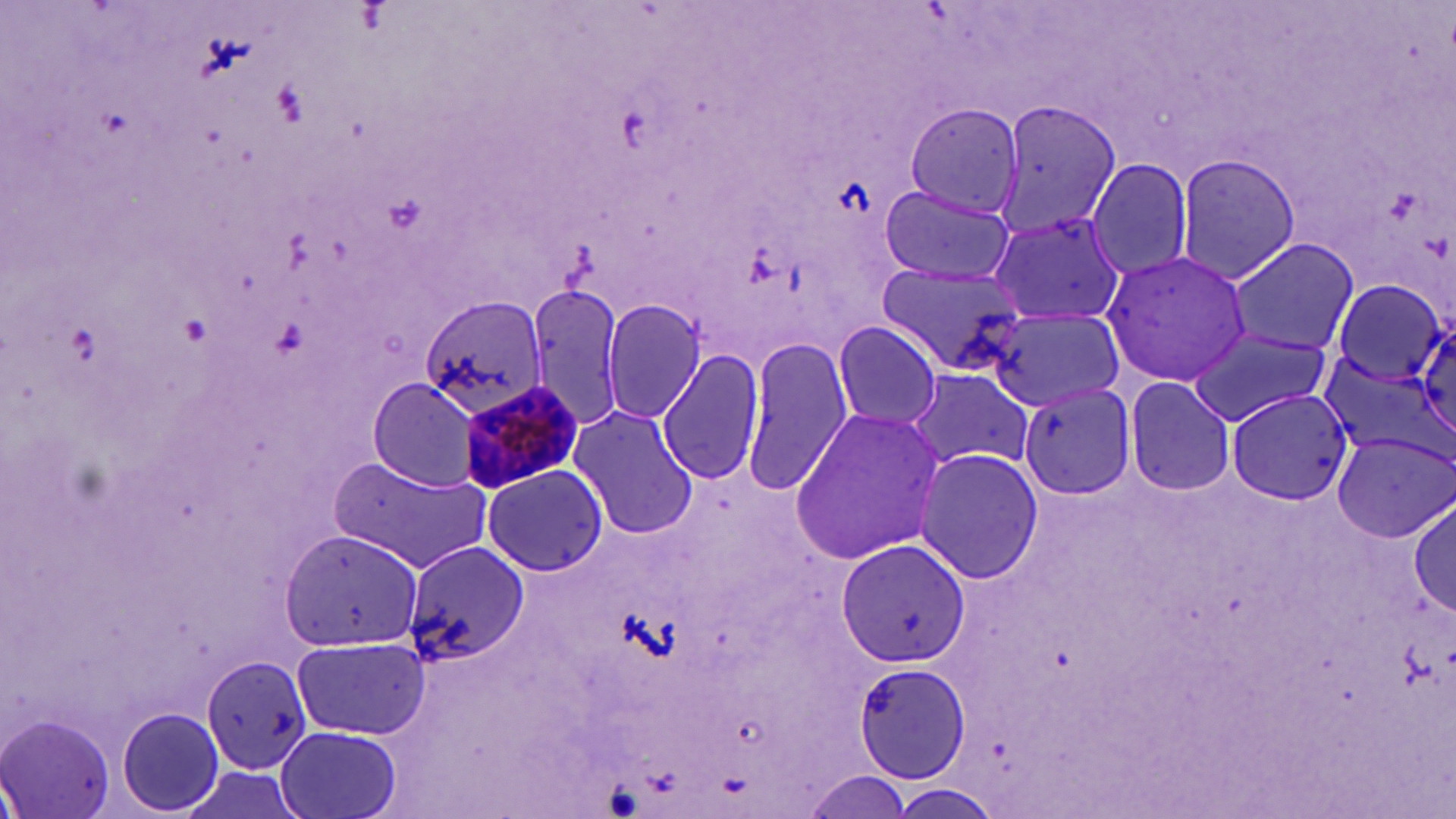 Approximate bounding boxes as [x1, y1, x2, y2] in pixels. Plasmodium malariae-infected red blood cell locations: [456, 379, 587, 496]. Uninfected red blood cell locations: [991, 98, 1120, 241], [903, 102, 1022, 220], [902, 104, 1023, 217], [1174, 153, 1301, 284], [1087, 157, 1195, 281], [879, 185, 1016, 285], [987, 210, 1126, 327], [1224, 237, 1357, 357], [1100, 250, 1252, 388], [875, 260, 1033, 378], [1330, 279, 1447, 385], [525, 282, 625, 432], [420, 294, 551, 418], [602, 299, 705, 422], [986, 305, 1126, 413], [1413, 317, 1456, 446], [832, 321, 943, 430], [1188, 328, 1332, 427], [739, 336, 853, 498], [659, 348, 765, 485], [904, 367, 1034, 477], [366, 377, 482, 493], [1125, 377, 1236, 496], [1018, 380, 1136, 500], [1224, 389, 1354, 506], [568, 404, 699, 539], [788, 406, 949, 567], [1331, 427, 1452, 540], [1334, 433, 1453, 543], [914, 448, 1043, 584], [330, 457, 491, 569], [477, 464, 610, 576], [1410, 499, 1455, 618], [280, 527, 423, 651], [834, 535, 970, 668], [402, 541, 529, 668], [290, 631, 430, 741], [202, 655, 313, 773], [853, 661, 973, 786], [115, 707, 225, 815], [0, 716, 115, 819], [273, 724, 403, 819], [799, 770, 913, 818]. Slide-level diagnosis: Plasmodium malariae. Image is 1456×819 pixels. Thin blood film. 1000x magnification. Optical microscopy. May-Grünwald-Giemsa stain. Single field of view.